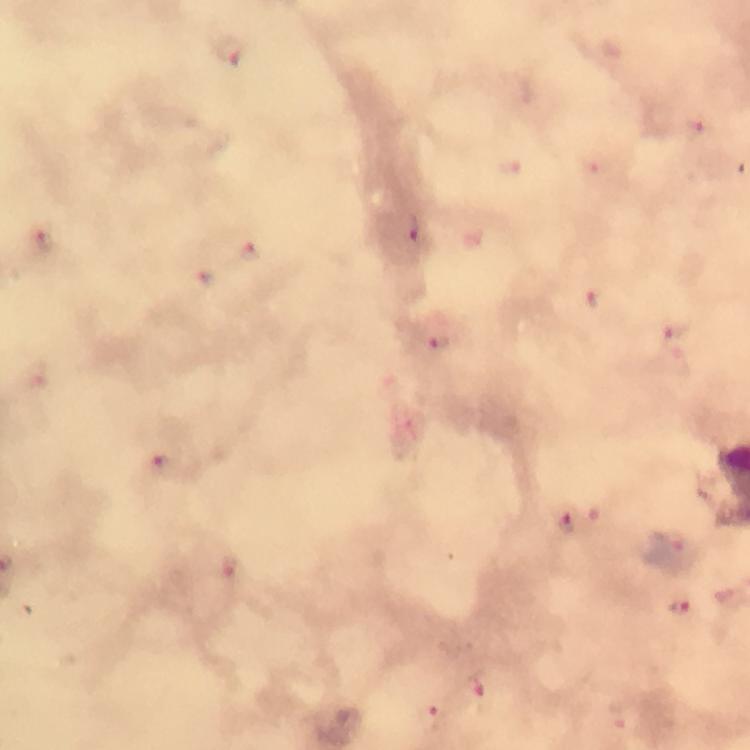
Approximate centers as [x, y] in pixels. Plasmodium parasite locations: [231, 50], [698, 127], [510, 164], [593, 165], [416, 230], [43, 240], [251, 252], [205, 277], [595, 301], [678, 330], [440, 344], [38, 373], [168, 467], [566, 523], [678, 543], [232, 565], [680, 608], [480, 688], [432, 718]. Immersion oil applied. Smartphone photograph taken through a microscope. Cropped region of a single field of view. From a diagnostic examination for malaria. Thick blood film. Image is 750×750 pixels. Giemsa-stained preparation. At 100x magnification.